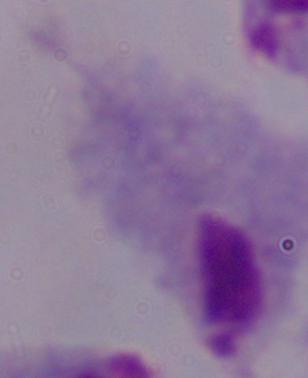
modality = photomicrograph
identification = trichomonad
magnification = 1000x